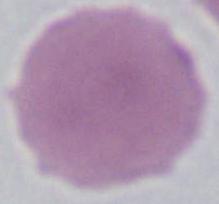
Summary:
  - Modality: photomicrograph
  - Magnification: 1000x
  - Identification: erythrocyte